Outline each uninfected red blood cell.
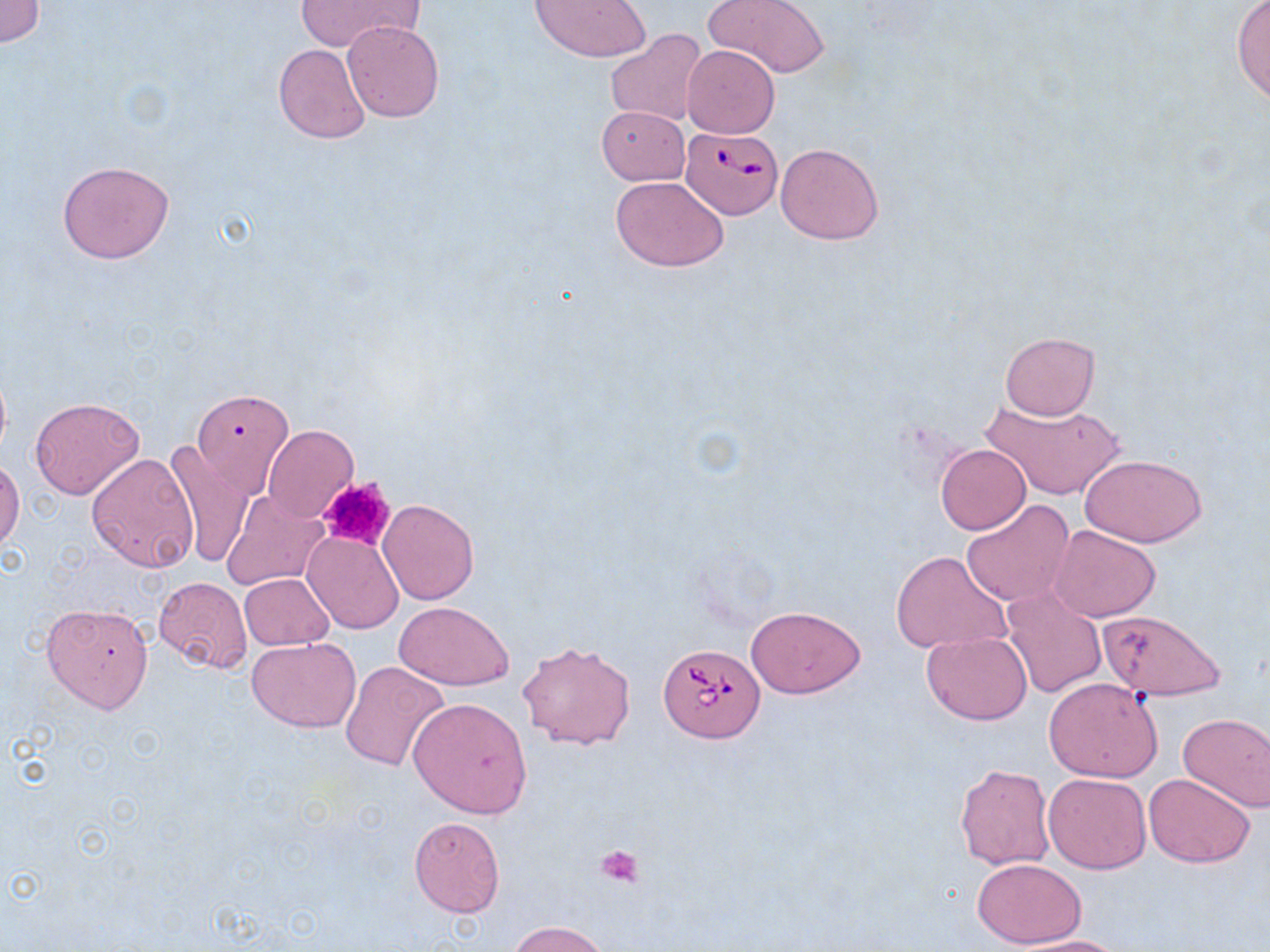
Approximate bounding boxes as named x1/y1/x2/y2 corners in pixels.
Uninfected red blood cells: (x1=294, y1=0, x2=421, y2=55), (x1=531, y1=0, x2=649, y2=61), (x1=705, y1=0, x2=831, y2=79), (x1=0, y1=1, x2=46, y2=47), (x1=1230, y1=1, x2=1270, y2=108), (x1=342, y1=20, x2=443, y2=122), (x1=606, y1=30, x2=713, y2=127), (x1=273, y1=43, x2=371, y2=143), (x1=682, y1=46, x2=779, y2=137), (x1=596, y1=106, x2=689, y2=185), (x1=774, y1=142, x2=885, y2=245), (x1=56, y1=161, x2=176, y2=264), (x1=610, y1=174, x2=729, y2=272), (x1=1001, y1=332, x2=1099, y2=420), (x1=188, y1=392, x2=294, y2=502), (x1=979, y1=392, x2=1126, y2=502), (x1=28, y1=396, x2=145, y2=500), (x1=262, y1=426, x2=358, y2=522), (x1=163, y1=440, x2=254, y2=570), (x1=936, y1=444, x2=1030, y2=533), (x1=87, y1=452, x2=200, y2=573), (x1=1079, y1=454, x2=1209, y2=547), (x1=0, y1=456, x2=24, y2=554), (x1=222, y1=490, x2=328, y2=590), (x1=377, y1=498, x2=479, y2=605), (x1=961, y1=501, x2=1074, y2=608), (x1=1049, y1=525, x2=1161, y2=623), (x1=303, y1=531, x2=403, y2=634), (x1=891, y1=549, x2=1011, y2=654), (x1=239, y1=573, x2=334, y2=651), (x1=153, y1=574, x2=253, y2=673), (x1=1000, y1=587, x2=1109, y2=698), (x1=41, y1=601, x2=155, y2=715), (x1=394, y1=602, x2=514, y2=689), (x1=746, y1=605, x2=864, y2=699), (x1=1096, y1=608, x2=1228, y2=702), (x1=922, y1=632, x2=1033, y2=724), (x1=247, y1=636, x2=361, y2=734), (x1=519, y1=640, x2=637, y2=750), (x1=340, y1=661, x2=449, y2=773), (x1=1043, y1=677, x2=1163, y2=783), (x1=407, y1=697, x2=532, y2=817), (x1=1179, y1=713, x2=1270, y2=812), (x1=954, y1=763, x2=1057, y2=871), (x1=1042, y1=773, x2=1151, y2=873), (x1=1144, y1=773, x2=1255, y2=868), (x1=407, y1=815, x2=506, y2=918), (x1=972, y1=858, x2=1087, y2=947), (x1=508, y1=919, x2=613, y2=952), (x1=1005, y1=935, x2=1134, y2=952).

slide_level_diagnosis: Babesia divergens
stain: May-Grünwald-Giemsa
preparation: thin blood film
platelet_locations: 'approximate bounding boxes as named x1/y1/x2/y2 corners in pixels: (x1=316, y1=475, x2=397, y2=553), (x1=595, y1=846, x2=644, y2=887)'
magnification: 1000x
modality: light microscopy
image_size: 1270×952 pixels
babesia_divergens_infected_red_blood_cell_locations: 'approximate bounding boxes as named x1/y1/x2/y2 corners in pixels: (x1=680, y1=126, x2=785, y2=218), (x1=659, y1=643, x2=764, y2=740)'
field_of_view: single